Assess this cell for malaria.
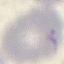
Uninfected.

Thin blood film. Automatically extracted cell patch, resized to 64 × 64 pixels. Photographed with a smartphone camera at the microscope eyepiece. Giemsa-stained preparation.